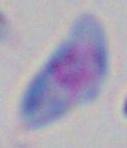

Toxoplasma gondii is seen. 1000x magnification. Photomicrograph.